Assess this cell for malaria.
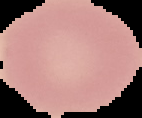

It is uninfected.

image size = 142×118 pixels
image type = cell region segmented out of the field of view; surrounding area masked to black
preparation = thin blood film